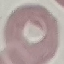

Summary:
  - Malaria status: uninfected
  - Stain: Giemsa
  - Image type: automatically extracted cell patch, resized to 64 × 64 pixels
  - Preparation: thin smear
  - Capture: smartphone through the microscope eyepiece